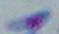

Summary:
  - Identification: Toxoplasma gondii
  - Magnification: 1000x
  - Modality: micrograph